Point out each leukocyte.
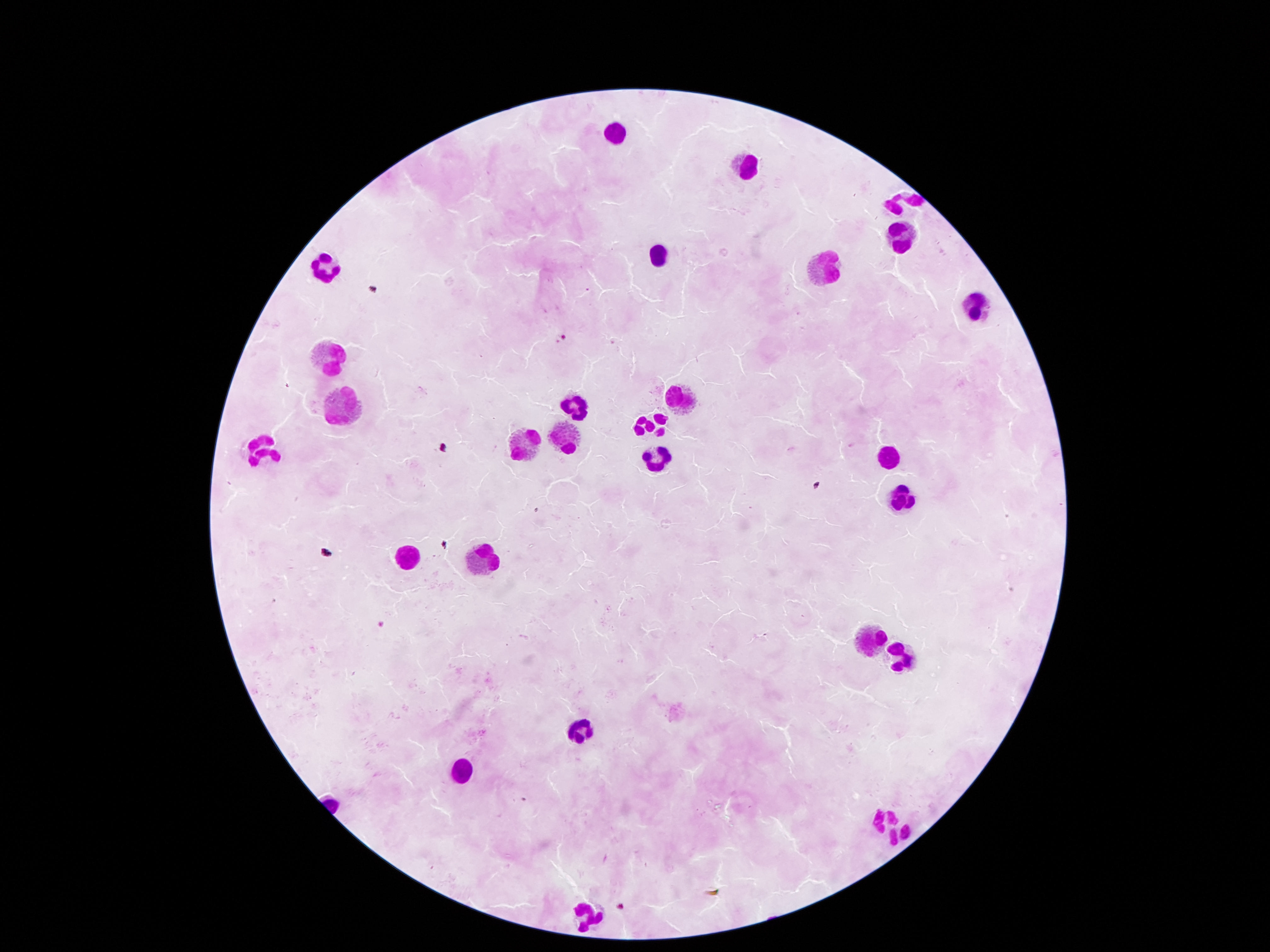

Approximate centers as [x, y] in pixels.
Leukocytes: [618, 134], [743, 165], [904, 204], [897, 235], [659, 255], [327, 264], [825, 271], [972, 307], [328, 359], [678, 391], [344, 403], [582, 406], [648, 425], [527, 446], [558, 446], [261, 448], [885, 452], [655, 453], [903, 498], [413, 556], [488, 557], [869, 634], [899, 654], [582, 729], [463, 766], [885, 817], [585, 913].

Summary:
  - Patient malaria status: not infected
  - Preparation: thick blood film
  - Field of view: single
  - Stain: Giemsa
  - Image size: 1270×952 pixels
  - Magnification: 100x
  - Capture: smartphone camera through the microscope eyepiece